State the preparation type.
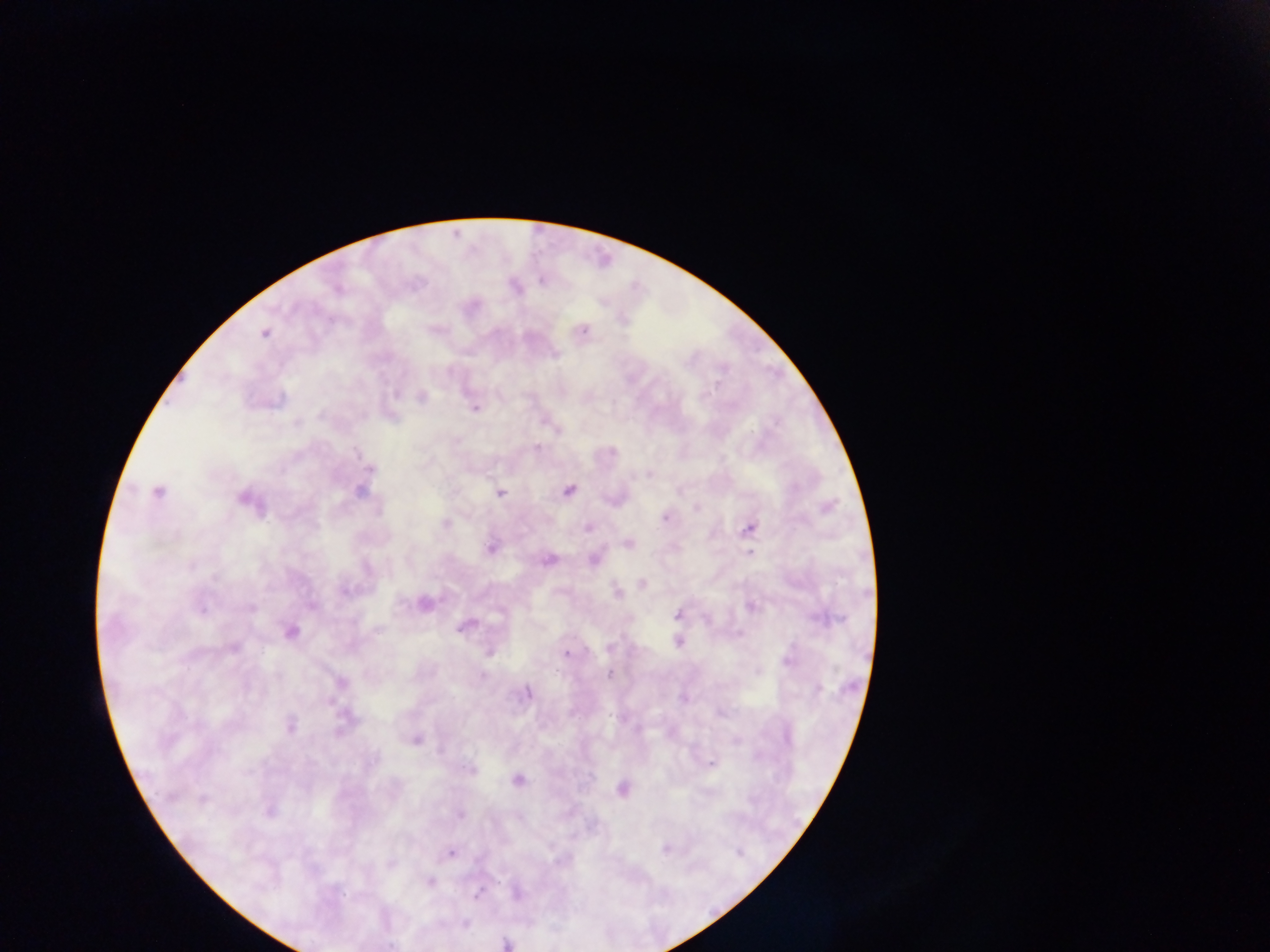
Thick blood film.

country = Ghana
image size = 1270×952 pixels
malaria parasite locations = approximate centers as (x, y) in pixels: (541, 280), (417, 285), (514, 287), (333, 323), (584, 329), (430, 330), (554, 356), (685, 358), (691, 358), (715, 385), (394, 393), (421, 395), (475, 408), (297, 424), (536, 447), (613, 449), (357, 454), (372, 470), (648, 474), (644, 476), (568, 488), (360, 491), (680, 491), (157, 493), (501, 494), (240, 499), (695, 507), (664, 518), (445, 524), (588, 527), (751, 527), (628, 544), (491, 547), (750, 550), (547, 559), (192, 564), (216, 578), (642, 582), (616, 592), (423, 606), (251, 608), (202, 609), (676, 614), (707, 619), (467, 622), (462, 627), (290, 631), (739, 633), (677, 641), (611, 646), (489, 653), (565, 653), (787, 662), (609, 674), (482, 677), (527, 692), (291, 727), (340, 730), (416, 739), (712, 764), (246, 773), (517, 780), (622, 788), (203, 799), (461, 814), (664, 850), (452, 852), (429, 882), (477, 894), (466, 923), (504, 943)
capture = mobile-phone photograph through a microscope
field of view = single